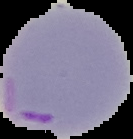

malaria_status: parasitized
image_size: 133×139 pixels
preparation: thin blood film
image_type: segmented cell region with the area outside set to black